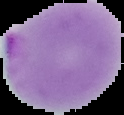 From a thin blood film. Image is 124×115 pixels. The area outside the segmented cell region is set to black. Result: Plasmodium parasites detected.